Locate every Plasmodium vivax-infected red blood cell.
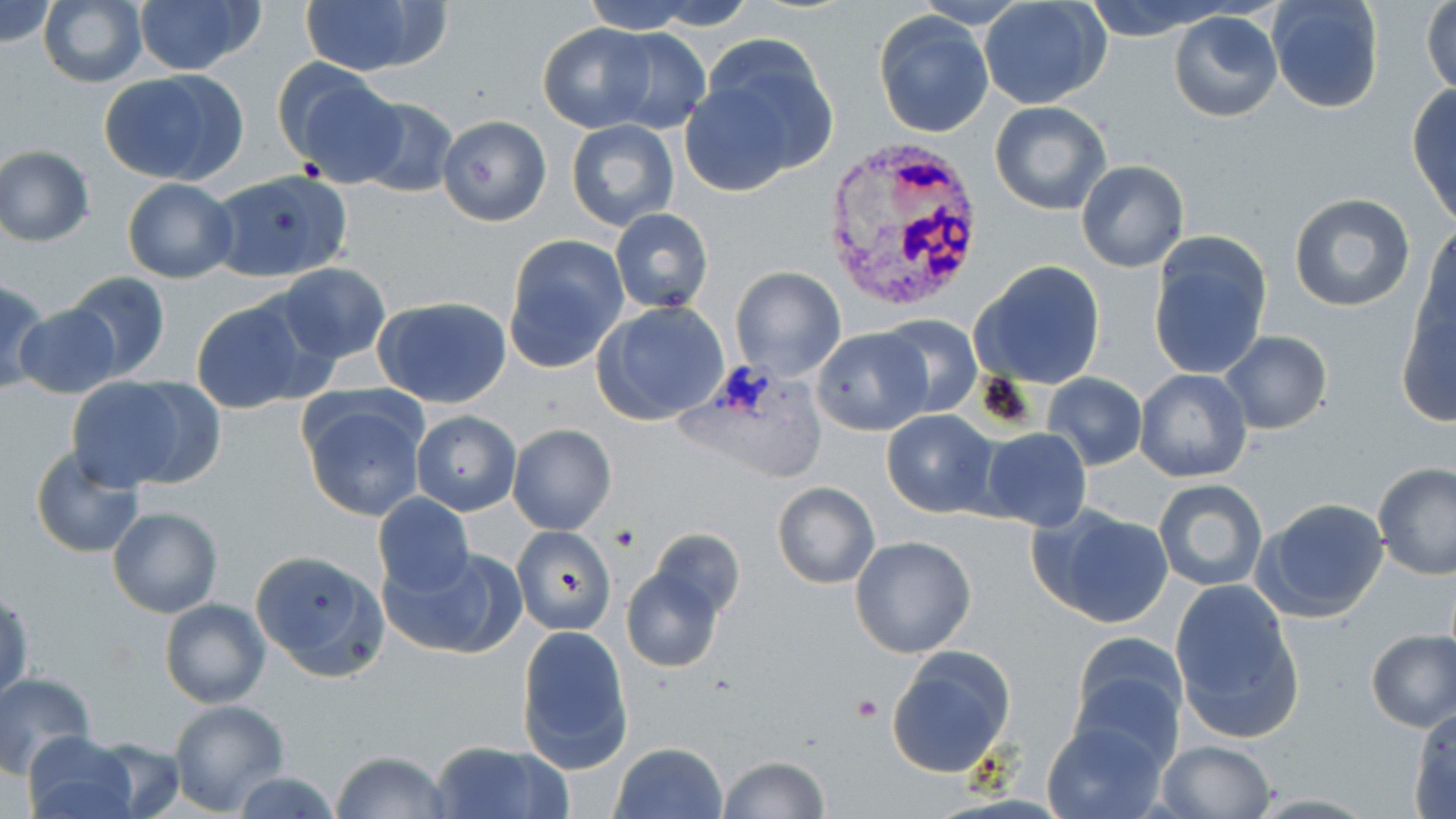

Approximate bounding boxes as [x1, y1, x2, y2] in pixels.
Plasmodium vivax-infected red blood cells: [821, 139, 989, 312].

slide-level diagnosis = Plasmodium vivax
modality = optical microscopy
stain = May-Grünwald-Giemsa
image size = 1456×819 pixels
preparation = thin blood film
uninfected red blood cell locations = approximate bounding boxes as [x1, y1, x2, y2] in pixels: [1, 0, 58, 47], [298, 0, 443, 76], [578, 0, 703, 33], [643, 0, 757, 31], [38, 1, 147, 87], [133, 1, 263, 76], [980, 1, 1110, 109], [1083, 1, 1233, 39], [1267, 1, 1383, 114], [1423, 2, 1456, 95], [873, 9, 996, 138], [1168, 11, 1282, 124], [537, 22, 658, 132], [601, 29, 711, 134], [685, 38, 840, 189], [278, 64, 403, 184], [99, 70, 247, 185], [1406, 84, 1456, 226], [352, 97, 458, 198], [989, 101, 1112, 216], [436, 115, 551, 226], [567, 119, 678, 231], [0, 145, 95, 245], [1076, 161, 1189, 273], [206, 170, 355, 283], [122, 177, 238, 284], [1289, 193, 1416, 312], [610, 208, 713, 314], [1417, 225, 1456, 346], [503, 234, 630, 373], [1147, 234, 1273, 380], [971, 261, 1107, 391], [271, 262, 393, 366], [730, 267, 846, 382], [63, 271, 170, 381], [0, 279, 49, 395], [190, 295, 316, 414], [373, 295, 513, 408], [1395, 299, 1456, 427], [594, 300, 733, 425], [14, 304, 122, 400], [875, 313, 981, 418], [811, 328, 932, 436], [1218, 330, 1332, 435], [1136, 368, 1253, 482], [1043, 374, 1147, 470], [118, 377, 228, 487], [62, 378, 196, 491], [1007, 384, 1138, 515], [298, 391, 428, 522], [412, 410, 520, 515], [881, 411, 997, 518], [507, 424, 616, 534], [978, 428, 1093, 531], [30, 447, 145, 560], [1374, 464, 1456, 582], [1153, 479, 1267, 591], [771, 482, 879, 588], [371, 492, 474, 596], [1254, 496, 1391, 622], [1030, 504, 1175, 630], [107, 506, 223, 618], [512, 526, 615, 636], [648, 528, 744, 619], [850, 535, 977, 658], [380, 547, 524, 661], [250, 549, 388, 680], [620, 566, 725, 673], [1171, 580, 1304, 742], [0, 591, 33, 703], [159, 598, 271, 708], [515, 625, 633, 771], [1365, 629, 1456, 732], [1069, 631, 1190, 761], [887, 646, 1016, 778], [0, 670, 97, 777], [168, 700, 289, 814], [1407, 704, 1456, 816], [1042, 717, 1168, 819], [23, 732, 139, 819], [90, 736, 185, 817], [427, 739, 569, 819], [1154, 740, 1276, 819], [609, 742, 727, 819], [330, 750, 452, 819], [716, 756, 832, 818], [228, 769, 342, 819]
field of view = single
magnification = 1000x
platelet locations = approximate bounding boxes as [x1, y1, x2, y2] in pixels: [853, 694, 883, 720]